Comment on the morphology of the red blood cells.
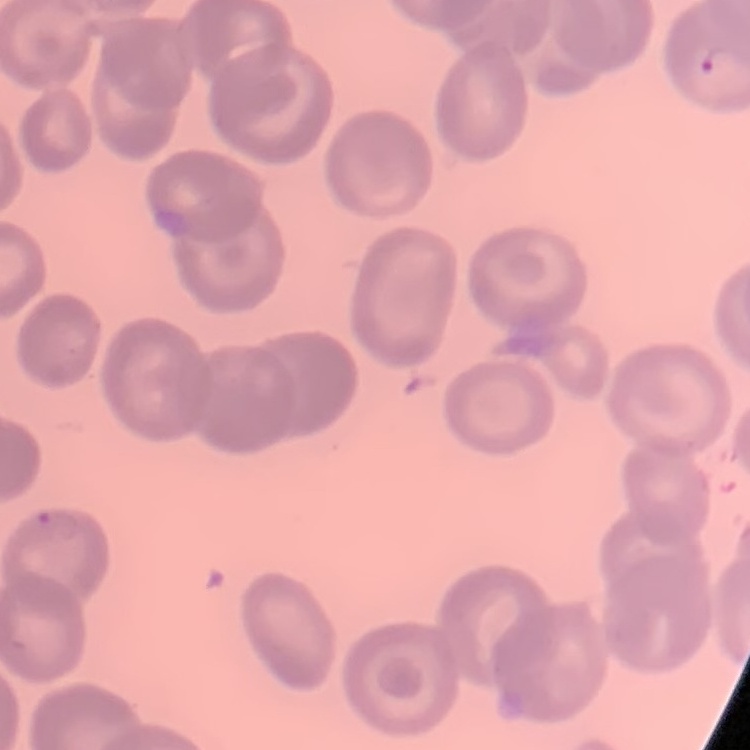
No rouleaux formation.

{
  "stain": "Field's or Giemsa",
  "image_type": "one tile cut from a larger photomicrograph",
  "preparation": "thin blood smear"
}